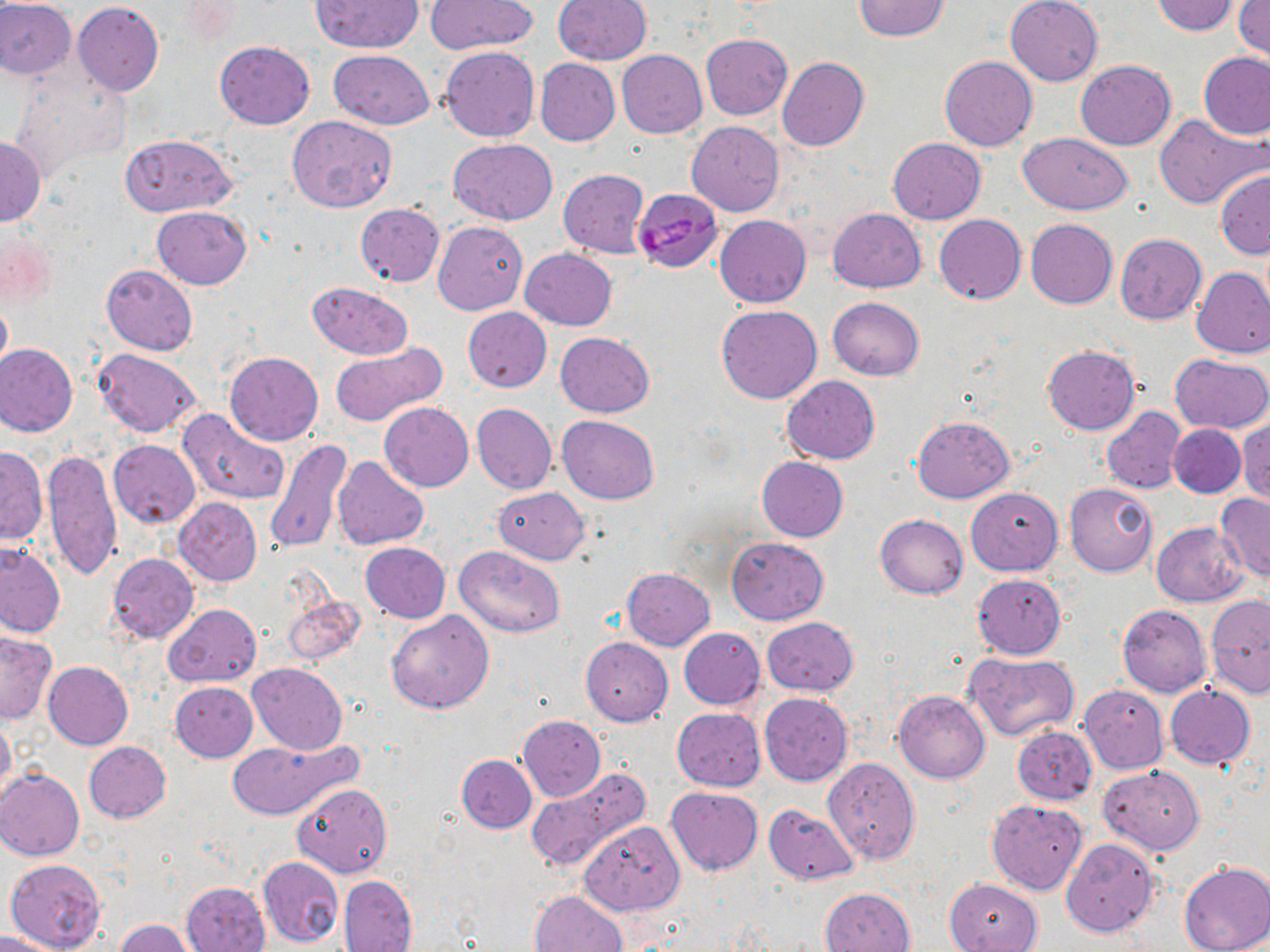

Plasmodium falciparum-infected red blood cell locations = approximate bounding boxes as [x1, y1, x2, y2] in pixels: [632, 188, 722, 273]
slide-level diagnosis = Plasmodium falciparum
magnification = 1000x
field of view = single
preparation = thin blood film
uninfected red blood cell locations = approximate bounding boxes as [x1, y1, x2, y2] in pixels: [0, 0, 75, 79], [310, 0, 424, 53], [553, 0, 652, 65], [851, 0, 952, 42], [1005, 0, 1103, 85], [425, 1, 538, 53], [1148, 1, 1238, 35], [72, 2, 163, 97], [1233, 2, 1270, 62], [701, 34, 792, 120], [215, 40, 315, 129], [439, 46, 540, 141], [617, 49, 707, 137], [327, 50, 435, 129], [1200, 52, 1269, 140], [939, 56, 1037, 151], [776, 57, 868, 151], [534, 58, 619, 146], [1075, 60, 1176, 150], [8, 70, 131, 178], [1154, 114, 1266, 209], [287, 115, 397, 213], [687, 121, 784, 216], [1018, 132, 1133, 213], [121, 134, 235, 217], [0, 136, 45, 224], [448, 138, 556, 224], [887, 138, 986, 224], [558, 169, 650, 258], [1215, 170, 1270, 260], [354, 204, 444, 286], [152, 206, 251, 290], [827, 207, 927, 292], [715, 214, 811, 308], [934, 214, 1026, 304], [1025, 219, 1117, 309], [433, 221, 528, 314], [1, 228, 54, 314], [1026, 228, 1204, 315], [1115, 234, 1207, 325], [521, 248, 616, 330], [101, 264, 197, 356], [1193, 266, 1270, 359], [306, 282, 413, 359], [316, 285, 425, 422], [0, 297, 11, 376], [827, 297, 925, 381], [717, 305, 822, 403], [461, 307, 551, 391], [555, 332, 655, 417], [329, 342, 448, 428], [1, 343, 78, 436], [1043, 345, 1139, 435], [93, 348, 201, 437], [225, 351, 323, 446], [1171, 353, 1270, 435], [782, 375, 880, 464], [379, 402, 473, 491], [472, 403, 556, 495], [1102, 406, 1188, 494], [178, 410, 288, 505], [557, 415, 658, 505], [912, 416, 1015, 503], [1236, 418, 1270, 506], [217, 423, 336, 532], [1169, 423, 1246, 498], [265, 439, 354, 555], [109, 440, 200, 528], [1, 447, 48, 544], [44, 448, 122, 581], [334, 456, 429, 549], [757, 456, 848, 541], [1065, 483, 1158, 577], [493, 486, 590, 564], [965, 487, 1063, 576], [1215, 494, 1270, 583], [174, 498, 263, 586], [875, 513, 968, 598], [1151, 522, 1248, 607], [726, 538, 830, 624], [0, 543, 65, 638], [361, 543, 450, 624], [455, 546, 566, 638], [107, 553, 199, 643], [622, 567, 715, 650], [972, 573, 1066, 659], [280, 591, 366, 666], [1205, 593, 1270, 699], [164, 603, 261, 687], [1117, 604, 1210, 697], [386, 610, 494, 714], [761, 617, 858, 696], [678, 628, 766, 709], [0, 631, 57, 724], [580, 636, 673, 726], [966, 651, 1081, 740], [43, 661, 133, 749], [247, 662, 347, 756], [170, 681, 258, 762], [1165, 684, 1255, 770], [1079, 685, 1168, 774], [894, 690, 990, 784], [760, 693, 851, 786], [672, 707, 766, 791], [0, 714, 17, 801], [517, 715, 606, 801], [1012, 726, 1098, 806], [228, 736, 361, 820], [84, 742, 172, 823], [456, 754, 536, 833], [823, 757, 920, 865], [1098, 765, 1205, 854], [525, 767, 651, 874], [1, 768, 84, 860], [293, 783, 393, 877], [666, 786, 762, 875], [987, 799, 1087, 895], [762, 804, 860, 886], [578, 821, 684, 917], [1061, 838, 1160, 937], [257, 857, 344, 948], [6, 858, 107, 952], [1179, 860, 1270, 952], [338, 875, 418, 952], [945, 878, 1042, 952], [182, 880, 271, 952], [820, 887, 916, 952], [529, 890, 628, 952], [118, 920, 196, 952], [0, 930, 60, 952]
modality = optical microscopy
image size = 1270×952 pixels
stain = May-Grünwald-Giemsa